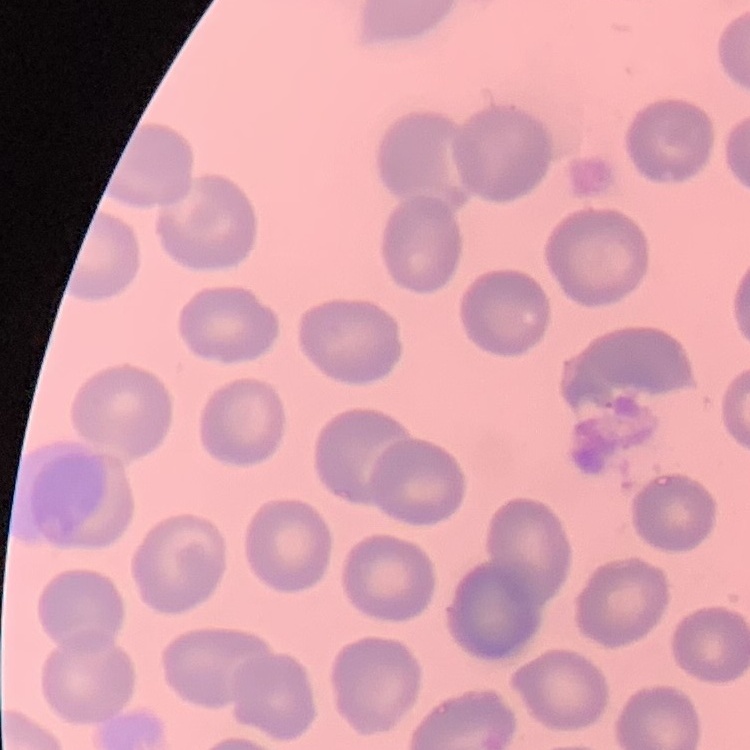

Summary:
  - Red blood cell morphology: no rouleaux formation
  - Preparation: thin blood film
  - Image type: square crop of a larger photomicrograph
  - Stain: Field's or Giemsa